Identify the blood parasite species.
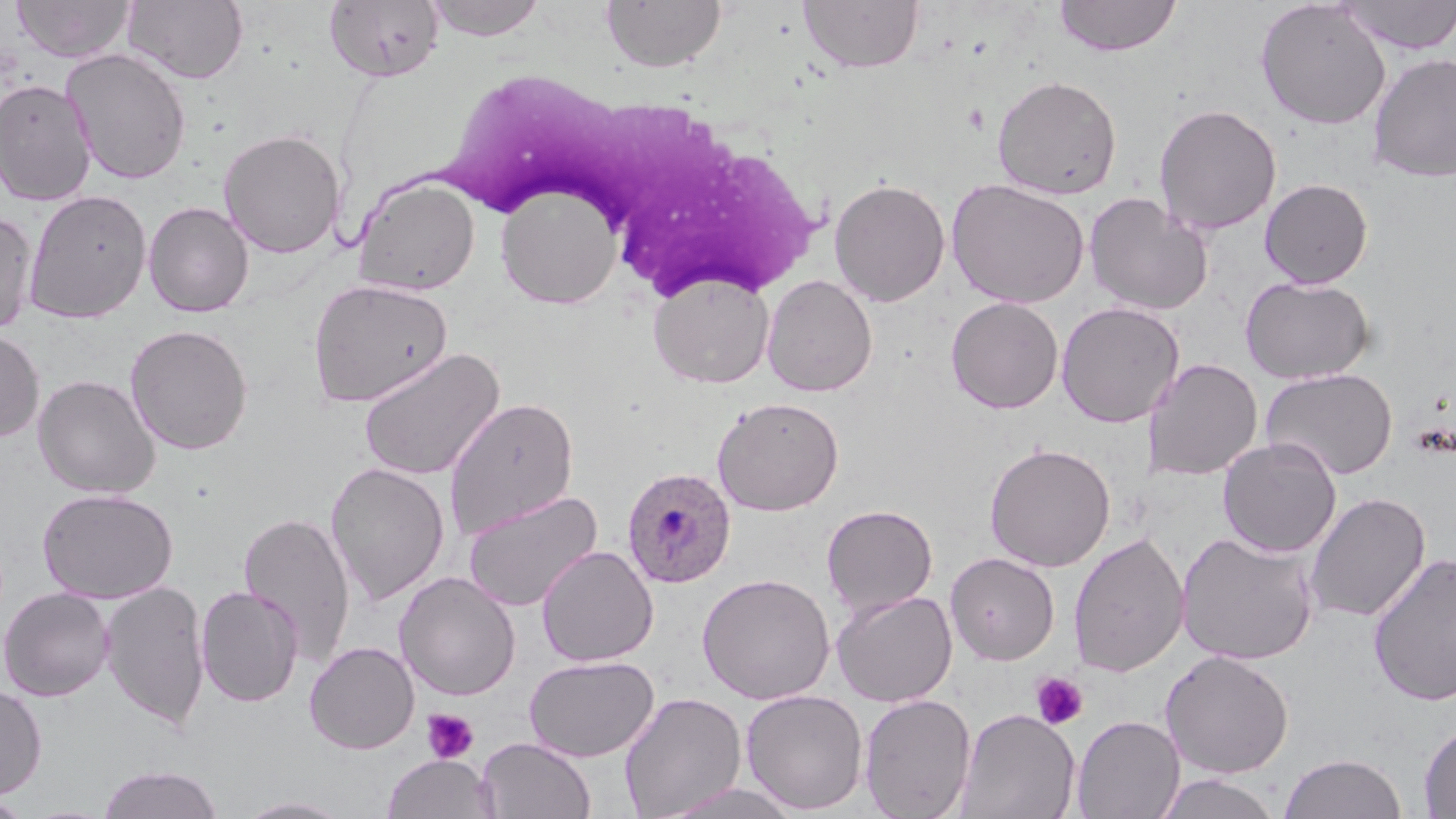
Plasmodium ovale.

Summary:
  - Coordinate format: approximate bounding boxes as named x1/y1/x2/y2 corners in pixels
  - White blood cell locations: (x1=440, y1=76, x2=827, y2=289)
  - Uninfected red blood cell locations: (x1=13, y1=0, x2=136, y2=63), (x1=425, y1=0, x2=548, y2=41), (x1=601, y1=0, x2=727, y2=73), (x1=799, y1=0, x2=923, y2=73), (x1=1054, y1=0, x2=1182, y2=57), (x1=1337, y1=0, x2=1456, y2=54), (x1=123, y1=1, x2=249, y2=84), (x1=324, y1=1, x2=445, y2=83), (x1=1255, y1=1, x2=1391, y2=130), (x1=61, y1=48, x2=193, y2=184), (x1=1368, y1=51, x2=1456, y2=183), (x1=992, y1=74, x2=1122, y2=199), (x1=0, y1=79, x2=97, y2=206), (x1=1154, y1=103, x2=1281, y2=236), (x1=217, y1=128, x2=346, y2=259), (x1=353, y1=176, x2=480, y2=296), (x1=829, y1=177, x2=951, y2=307), (x1=946, y1=178, x2=1090, y2=309), (x1=1259, y1=178, x2=1374, y2=289), (x1=495, y1=182, x2=623, y2=309), (x1=24, y1=189, x2=151, y2=323), (x1=1083, y1=192, x2=1213, y2=315), (x1=143, y1=201, x2=255, y2=318), (x1=0, y1=209, x2=38, y2=337), (x1=648, y1=272, x2=775, y2=389), (x1=762, y1=275, x2=878, y2=396), (x1=1240, y1=275, x2=1375, y2=385), (x1=308, y1=278, x2=453, y2=408), (x1=946, y1=296, x2=1064, y2=413), (x1=1056, y1=301, x2=1184, y2=428), (x1=125, y1=324, x2=253, y2=455), (x1=0, y1=328, x2=44, y2=442), (x1=357, y1=346, x2=505, y2=482), (x1=1142, y1=358, x2=1263, y2=481), (x1=1260, y1=367, x2=1398, y2=481), (x1=33, y1=374, x2=160, y2=498), (x1=443, y1=395, x2=579, y2=540), (x1=712, y1=396, x2=844, y2=515), (x1=1217, y1=437, x2=1342, y2=557), (x1=984, y1=442, x2=1116, y2=571), (x1=325, y1=461, x2=450, y2=607), (x1=37, y1=488, x2=178, y2=603), (x1=462, y1=489, x2=603, y2=613), (x1=1304, y1=491, x2=1430, y2=623), (x1=822, y1=504, x2=938, y2=617), (x1=238, y1=511, x2=356, y2=667), (x1=1067, y1=531, x2=1190, y2=679), (x1=1176, y1=531, x2=1319, y2=667), (x1=537, y1=544, x2=658, y2=667), (x1=945, y1=551, x2=1059, y2=665), (x1=1367, y1=552, x2=1456, y2=707), (x1=393, y1=571, x2=522, y2=701), (x1=697, y1=572, x2=836, y2=705), (x1=100, y1=581, x2=210, y2=731), (x1=195, y1=585, x2=304, y2=708), (x1=0, y1=587, x2=115, y2=702), (x1=831, y1=589, x2=957, y2=707), (x1=304, y1=641, x2=419, y2=754), (x1=1160, y1=650, x2=1294, y2=779), (x1=524, y1=655, x2=660, y2=762), (x1=0, y1=682, x2=47, y2=803), (x1=740, y1=689, x2=869, y2=814), (x1=619, y1=691, x2=747, y2=818), (x1=859, y1=693, x2=976, y2=819), (x1=956, y1=708, x2=1081, y2=819), (x1=1071, y1=715, x2=1185, y2=818), (x1=1419, y1=723, x2=1456, y2=817), (x1=477, y1=737, x2=596, y2=819), (x1=382, y1=753, x2=498, y2=819), (x1=1279, y1=753, x2=1407, y2=818), (x1=96, y1=764, x2=225, y2=819), (x1=1153, y1=772, x2=1283, y2=819), (x1=659, y1=781, x2=804, y2=819), (x1=0, y1=794, x2=32, y2=818), (x1=236, y1=796, x2=357, y2=818)
  - Platelet locations: (x1=1030, y1=671, x2=1089, y2=730), (x1=421, y1=708, x2=479, y2=764)
  - Plasmodium ovale-infected red blood cell locations: (x1=621, y1=466, x2=736, y2=589)
  - Modality: optical microscopy
  - Magnification: 1000x
  - Stain: May-Grünwald-Giemsa
  - Image size: 1456×819 pixels
  - Preparation: thin blood smear
  - Field of view: one of a larger specimen